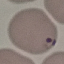

Summary:
  - Malaria status: parasitized
  - Capture: smartphone through the microscope eyepiece
  - Image type: automatically extracted cell patch, resized to 64 × 64 pixels
  - Preparation: thin blood film
  - Stain: Giemsa